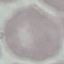
Result: no malaria parasites seen. Thin smear of blood. Giemsa stain. Automatically extracted cell patch, resized to 64 × 64 pixels. Photographed with a smartphone camera at the microscope eyepiece.